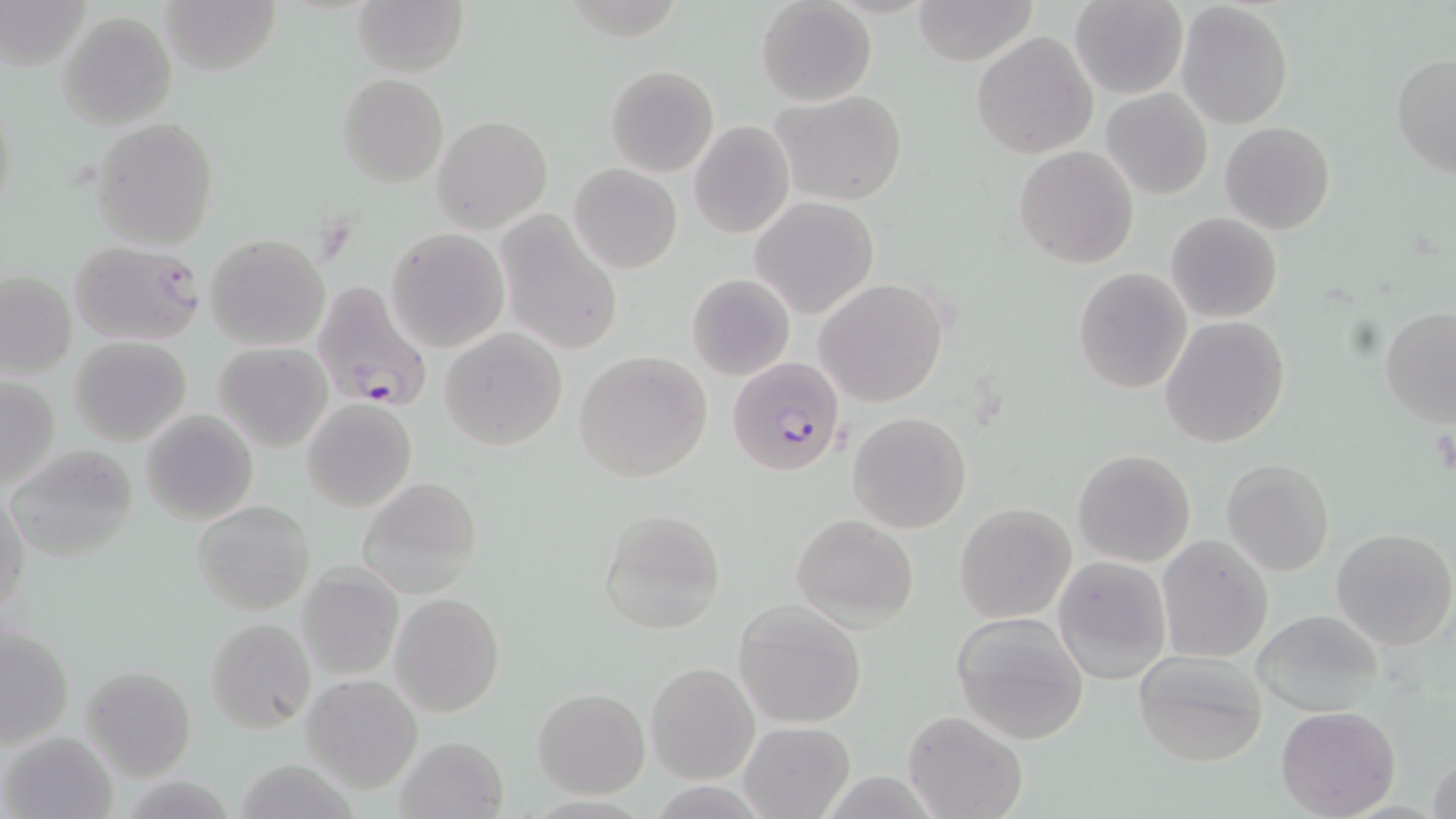

Approximate bounding boxes as (x1,y1)-(x2,y2) corner pairs in pixels. Plasmodium falciparum-infected red blood cell locations: (311,280)-(432,410), (727,356)-(847,476). Platelet locations: (1432,418)-(1455,477). Uninfected red blood cell locations: (1,0)-(90,71), (159,0)-(283,74), (353,0)-(468,77), (756,0)-(877,106), (911,0)-(1040,67), (1070,0)-(1188,100), (1175,2)-(1294,129), (58,10)-(177,129), (971,30)-(1097,159), (1390,52)-(1456,178), (605,65)-(720,177), (338,73)-(448,187), (1102,87)-(1213,200), (768,90)-(909,207), (91,116)-(219,249), (432,116)-(552,233), (688,120)-(795,239), (1220,121)-(1336,235), (1014,145)-(1139,268), (570,163)-(683,273), (751,198)-(877,318), (497,212)-(623,354), (1165,212)-(1282,322), (386,228)-(510,352), (206,234)-(329,349), (68,240)-(206,346), (1072,266)-(1194,393), (1,273)-(76,379), (688,273)-(794,380), (815,278)-(951,407), (1380,307)-(1456,425), (1161,316)-(1292,448), (440,327)-(568,449), (71,337)-(191,444), (214,342)-(332,452), (573,350)-(714,483), (0,375)-(60,489), (302,398)-(417,512), (141,411)-(257,524), (849,411)-(970,533), (6,448)-(139,561), (1073,449)-(1196,566), (1223,458)-(1335,576), (357,476)-(481,598), (2,491)-(29,617), (191,500)-(317,616), (953,502)-(1076,623), (598,507)-(727,634), (790,515)-(917,629), (1331,526)-(1456,651), (1157,535)-(1272,663), (1054,556)-(1171,684), (298,565)-(404,680), (391,592)-(504,716), (733,601)-(866,728), (1251,608)-(1388,715), (951,612)-(1091,744), (206,617)-(315,734), (2,624)-(74,751), (1132,651)-(1270,768), (646,662)-(758,783), (81,665)-(196,779), (302,674)-(423,793), (532,688)-(650,799), (1275,705)-(1400,818), (904,711)-(1026,819), (739,722)-(855,818), (3,730)-(114,818), (395,734)-(509,819), (1429,752)-(1455,819), (231,759)-(366,818). Slide-level diagnosis: Plasmodium falciparum. 1000x magnification. Thin blood smear. One field of a larger specimen. May-Grünwald-Giemsa stain. Image is 1456×819 pixels. Optical microscopy.